Assess the morphology of the red blood cells.
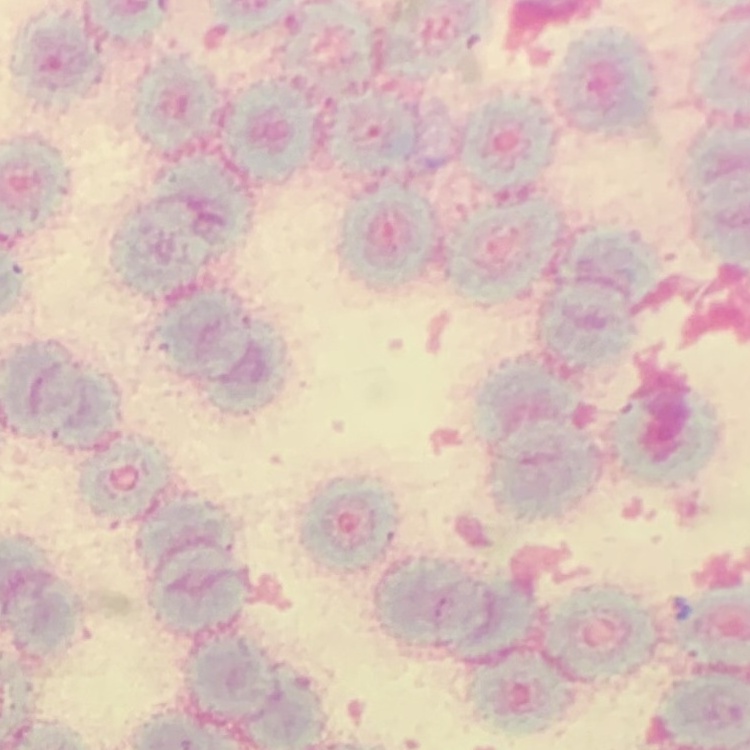
They show rouleaux formation.

stain = Field's or Giemsa
preparation = thin blood smear
image type = one tile cut from a larger photomicrograph